Outline each Plasmodium vivax-infected red blood cell.
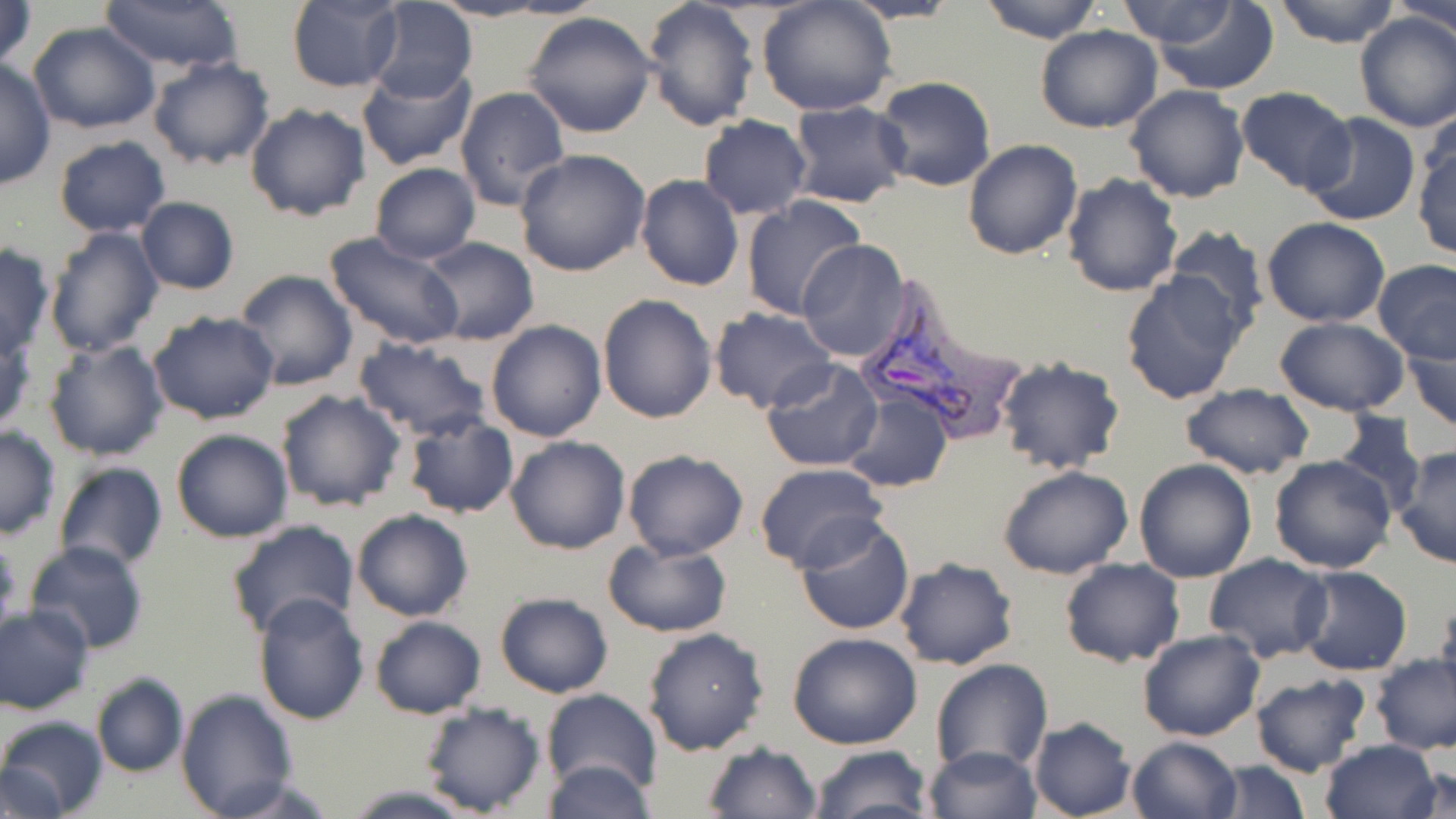
Approximate bounding boxes as [x1, y1, x2, y2] in pixels.
Plasmodium vivax-infected red blood cells: [850, 284, 1029, 452].

Uninfected red blood cell locations: [0, 0, 37, 74], [430, 0, 556, 21], [498, 0, 611, 19], [641, 0, 760, 133], [756, 0, 896, 117], [839, 0, 964, 24], [976, 0, 1108, 43], [1273, 0, 1401, 48], [1385, 0, 1456, 35], [103, 1, 243, 72], [285, 1, 405, 91], [365, 1, 477, 103], [1106, 1, 1248, 47], [1142, 3, 1282, 92], [1352, 10, 1456, 132], [522, 11, 658, 138], [27, 21, 160, 134], [1035, 25, 1163, 132], [146, 56, 275, 171], [0, 59, 55, 192], [357, 65, 476, 171], [873, 76, 997, 193], [1124, 84, 1252, 203], [455, 85, 572, 213], [1235, 87, 1356, 196], [786, 101, 911, 207], [245, 103, 373, 222], [1301, 113, 1421, 225], [697, 115, 813, 219], [53, 135, 171, 237], [1412, 137, 1455, 261], [963, 138, 1083, 259], [513, 150, 652, 279], [369, 163, 480, 265], [1061, 172, 1184, 297], [635, 174, 744, 291], [740, 193, 868, 320], [135, 196, 239, 294], [1262, 217, 1390, 327], [1164, 224, 1270, 341], [43, 225, 165, 358], [322, 231, 466, 350], [418, 236, 541, 346], [797, 239, 911, 362], [0, 244, 54, 362], [1372, 259, 1456, 363], [234, 269, 360, 392], [1120, 271, 1248, 406], [597, 293, 718, 424], [710, 308, 838, 414], [147, 310, 279, 425], [1272, 317, 1410, 417], [484, 320, 607, 441], [0, 326, 37, 439], [1404, 327, 1455, 434], [42, 338, 168, 461], [356, 338, 491, 443], [996, 357, 1128, 476], [759, 359, 884, 472], [1180, 383, 1316, 480], [275, 388, 407, 513], [841, 388, 952, 493], [1329, 412, 1428, 519], [402, 414, 519, 519], [0, 424, 60, 539], [171, 427, 294, 544], [505, 436, 632, 555], [1394, 446, 1456, 569], [622, 449, 750, 560], [1269, 454, 1398, 573], [1133, 458, 1257, 583], [53, 460, 168, 572], [753, 463, 888, 572], [997, 466, 1136, 580], [351, 509, 473, 622], [795, 515, 916, 637], [224, 519, 362, 641], [0, 535, 22, 644], [602, 537, 732, 636], [25, 541, 152, 656], [1203, 553, 1333, 661], [893, 557, 1020, 671], [1059, 559, 1186, 668], [1294, 565, 1414, 676], [253, 590, 372, 724], [494, 592, 613, 698], [1435, 593, 1456, 703], [0, 605, 95, 714], [371, 616, 486, 719], [641, 627, 769, 757], [1137, 629, 1266, 742], [787, 633, 923, 750], [1371, 654, 1456, 755], [930, 658, 1054, 775], [1249, 672, 1371, 779], [89, 673, 188, 777], [175, 689, 299, 817], [543, 689, 661, 800], [416, 701, 547, 817], [0, 716, 107, 819], [1028, 717, 1138, 819], [1126, 736, 1242, 819], [1318, 738, 1442, 819], [701, 742, 823, 819], [808, 744, 931, 819], [923, 745, 1042, 819], [540, 758, 655, 819], [1208, 761, 1310, 817], [1404, 761, 1454, 815], [1, 764, 65, 816], [339, 786, 480, 818]. Slide-level diagnosis: Plasmodium vivax. One field of a larger specimen. Image is 1456×819 pixels. Thin blood film. May-Grünwald-Giemsa-stained preparation. Captured at 1000x magnification. Optical microscopy.